Comment on the morphology of the red blood cells.
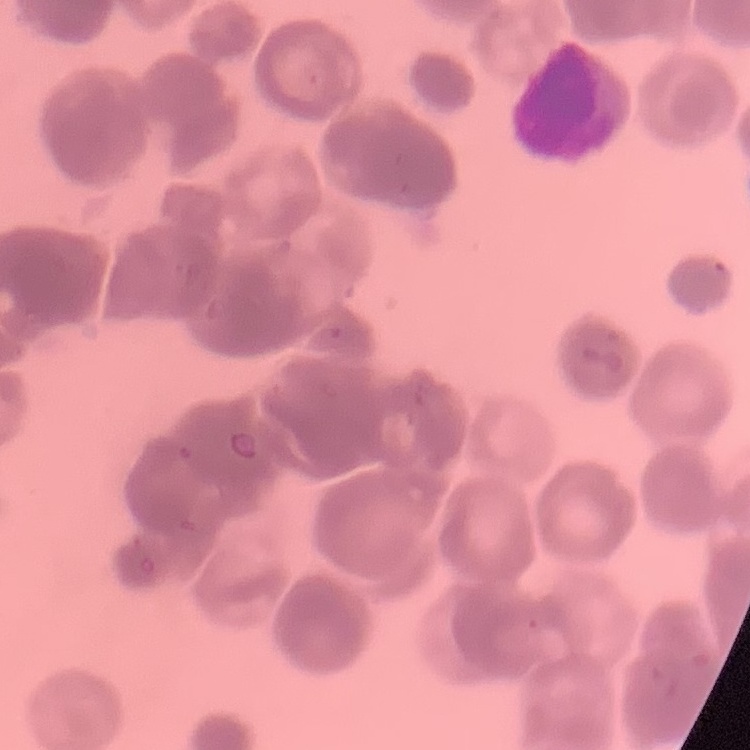
Rouleaux formation.

Summary:
  - Image type: square crop of a larger photomicrograph
  - Stain: Field's or Giemsa
  - Preparation: thin blood film